Describe the morphology of the erythrocytes.
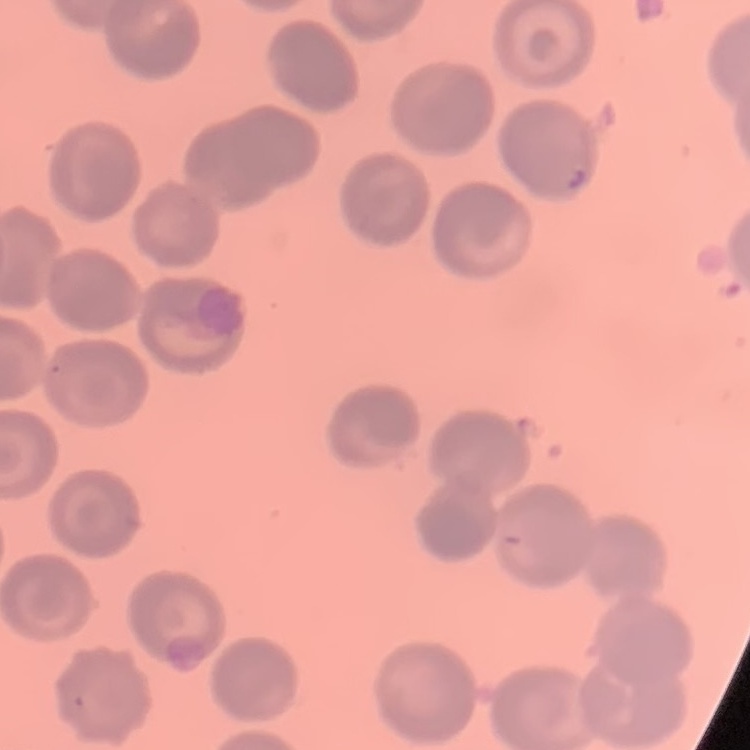
They show no rouleaux formation.

Summary:
  - Preparation: thin peripheral smear
  - Image type: square crop of a larger photomicrograph
  - Stain: Field's or Giemsa